Give the extent of all Plasmodium ovale-infected red blood cells.
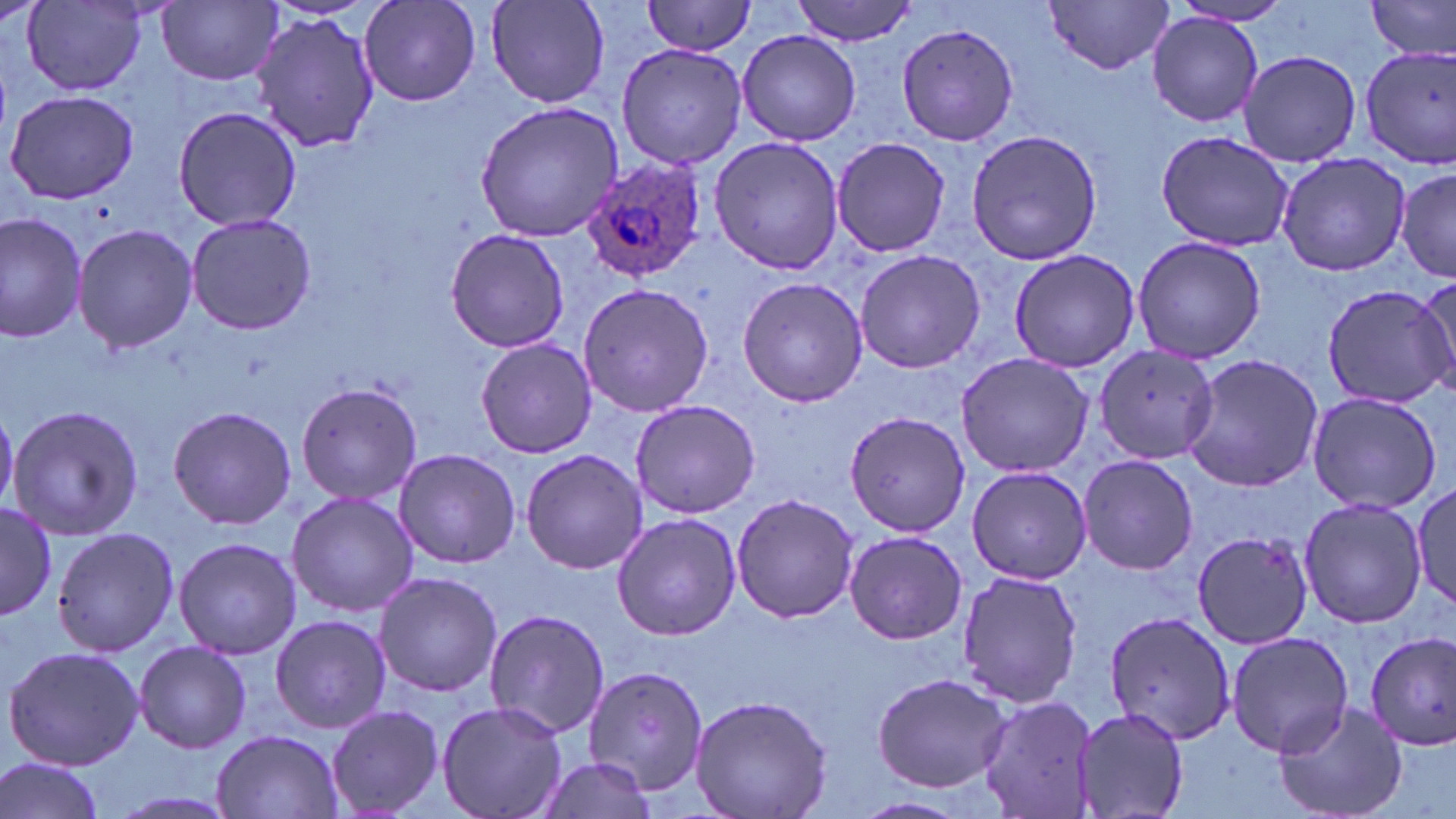

Approximate bounding boxes as (x1, y1, x2, y2) in pixels.
Plasmodium ovale-infected red blood cells: (580, 155, 709, 282).

Summary:
  - Uninfected red blood cell locations: (22, 0, 152, 94), (357, 0, 485, 108), (484, 0, 613, 109), (791, 0, 918, 45), (1368, 0, 1456, 62), (159, 1, 282, 86), (643, 1, 761, 55), (1043, 1, 1175, 73), (1167, 1, 1296, 27), (251, 12, 380, 153), (1147, 14, 1264, 128), (898, 22, 1022, 146), (735, 29, 863, 146), (615, 41, 747, 171), (1357, 44, 1456, 169), (1238, 49, 1361, 168), (3, 89, 139, 204), (476, 101, 624, 241), (173, 103, 301, 232), (965, 128, 1103, 266), (1154, 131, 1293, 251), (709, 135, 845, 274), (831, 136, 951, 259), (1276, 152, 1410, 277), (1395, 165, 1454, 283), (184, 211, 316, 338), (0, 212, 89, 342), (73, 222, 197, 354), (445, 228, 570, 353), (1130, 236, 1267, 365), (1008, 248, 1142, 372), (854, 249, 986, 374), (1414, 276, 1454, 398), (737, 277, 869, 409), (578, 280, 714, 418), (1322, 282, 1456, 407), (475, 336, 596, 459), (1092, 345, 1217, 463), (956, 351, 1096, 478), (1179, 352, 1324, 494), (296, 383, 423, 503), (1306, 390, 1442, 515), (629, 398, 762, 519), (7, 405, 146, 541), (167, 405, 297, 530), (843, 405, 974, 556), (392, 447, 520, 569), (519, 448, 651, 574), (1077, 455, 1200, 576), (966, 465, 1094, 585), (1410, 482, 1456, 611), (285, 491, 417, 618), (730, 493, 860, 625), (1298, 496, 1428, 629), (0, 501, 56, 625), (611, 512, 740, 641), (52, 526, 179, 657), (1191, 530, 1316, 649), (842, 531, 970, 645), (172, 536, 301, 661), (955, 568, 1083, 709), (373, 570, 504, 697), (481, 608, 610, 740), (1103, 610, 1238, 744), (268, 614, 392, 735), (1364, 629, 1455, 750), (1225, 632, 1353, 756), (133, 640, 254, 754), (4, 646, 146, 772), (582, 661, 711, 792), (870, 671, 1012, 791), (977, 692, 1100, 819), (690, 693, 834, 819), (1273, 699, 1409, 819), (435, 700, 568, 819), (325, 704, 444, 818), (1074, 706, 1190, 819), (212, 729, 345, 819), (0, 754, 107, 819), (530, 757, 659, 816), (850, 795, 981, 819)
  - Slide-level diagnosis: Plasmodium ovale
  - Magnification: 1000x
  - Modality: optical microscopy
  - Preparation: thin blood smear
  - Image size: 1456×819 pixels
  - Field of view: one of a larger specimen
  - Stain: May-Grünwald-Giemsa